State which parasite is depicted.
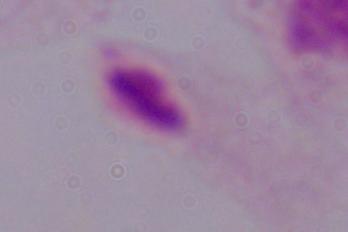
This is a trichomonad.

{
  "modality": "micrograph",
  "magnification": "1000x"
}